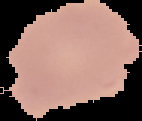
Malaria status: uninfected. Image is 142×121 pixels. From a thin blood smear. Segmented cell region on a black background.